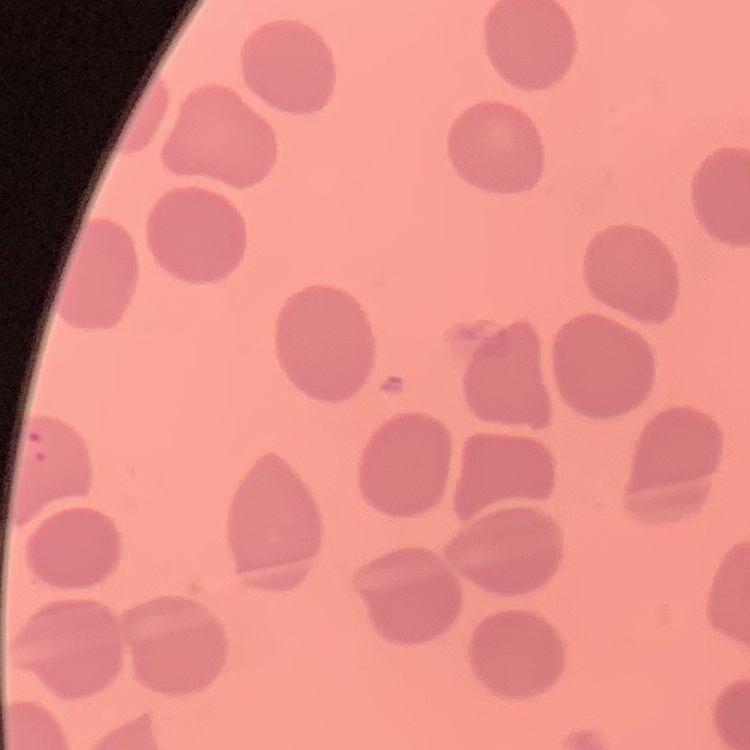

The red blood cells show no rouleaux formation. Field's or Giemsa stain. Thin blood film. One tile cut from a larger photomicrograph.